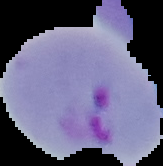
Summary:
  - Image type: segmented cell region with the area outside set to black
  - Malaria status: parasitized
  - Preparation: thin blood film
  - Image size: 163×166 pixels